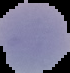 Cell region segmented out of the field of view; the surrounding area is masked to black. Result: negative for malaria parasites. Image is 70×73 pixels. From a thin blood film.